Locate every Plasmodium parasite.
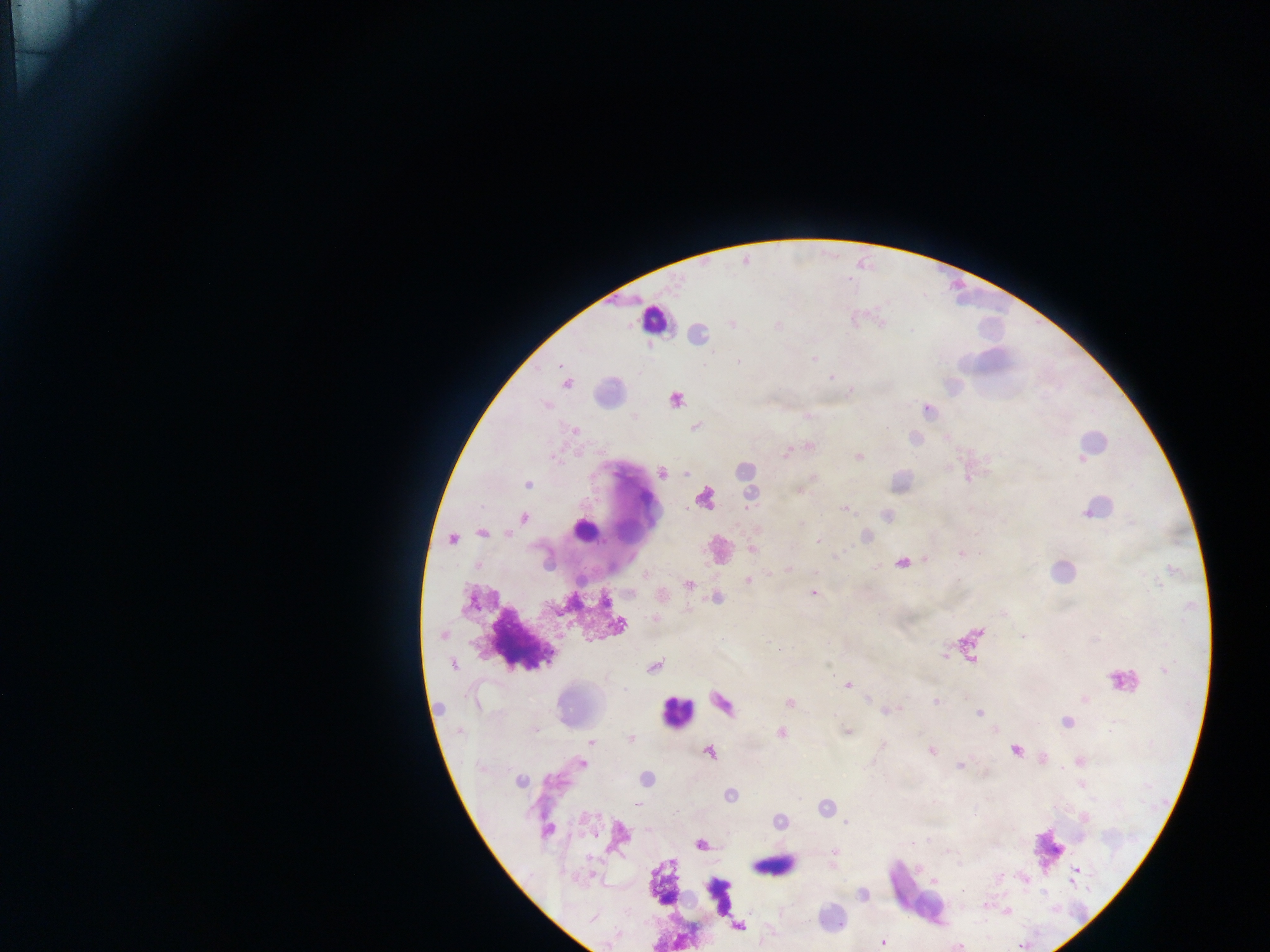

Approximate centers as x y in pixels.
Plasmodium parasites: 732 323; 814 359; 738 362; 560 365; 639 372; 831 377; 567 383; 851 391; 676 399; 634 417; 696 426; 575 430; 810 446; 787 453; 859 457; 662 473; 686 473; 527 485; 799 491; 845 509; 524 517; 802 524; 481 533; 507 534; 452 539; 819 541; 752 548; 961 554; 902 563; 815 572; 748 580; 688 584; 813 592; 604 602; 655 619; 620 626; 443 635; 1022 636; 944 655; 454 665; 654 667; 1165 670; 848 685; 1085 699; 937 701; 790 703; 890 710; 978 713; 1066 722; 534 730; 459 732; 780 732; 847 732; 631 738; 591 742; 1015 750; 932 751; 709 753; 582 763; 960 765; 646 778; 519 781; 730 795; 637 803; 846 823; 547 831; 912 843; 700 845; 834 852; 1077 870; 935 882; 862 895; 592 919; 739 926; 883 942.

image_size: 1270×952 pixels
field_of_view: single
leukocyte_locations: 'approximate centers as x y in pixels: 654 319; 583 531; 517 640; 1124 679; 677 711; 1045 851; 771 862; 716 894'
capture: mobile-phone photograph through a microscope
country: Ghana
preparation: thick blood smear